Give the position of every Plasmodium parasite.
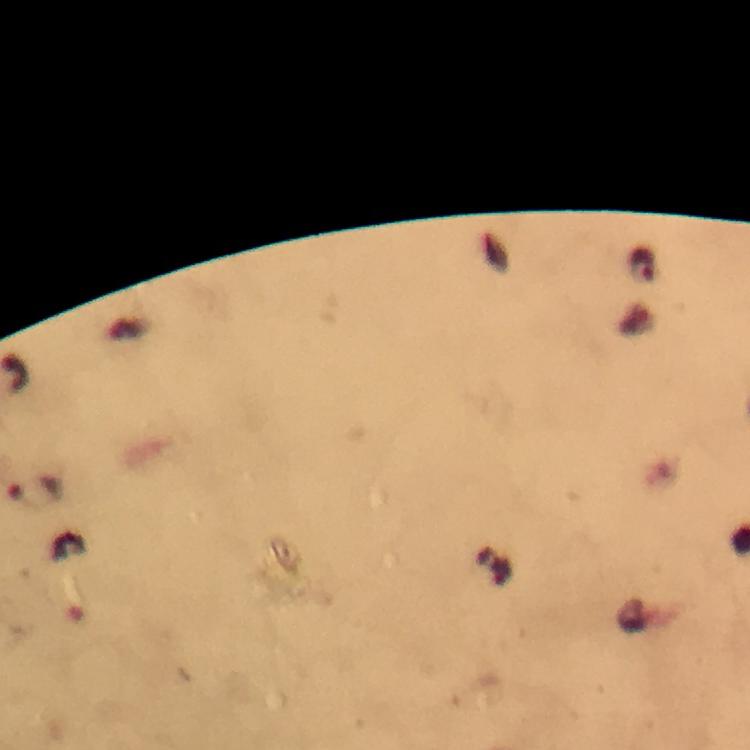

Approximate centers as [x, y] in pixels.
Plasmodium parasites: [643, 266], [38, 492].

preparation = thick blood film
stain = Giemsa
magnification = 100x
context = from a diagnostic examination for malaria
image size = 750×750 pixels
capture = smartphone mounted on the microscope
immersion oil = applied
cropped from = a single field of view